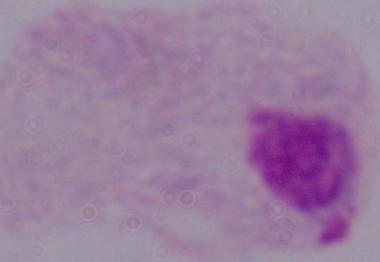
magnification = 1000x
identification = trichomonad
modality = photomicrograph